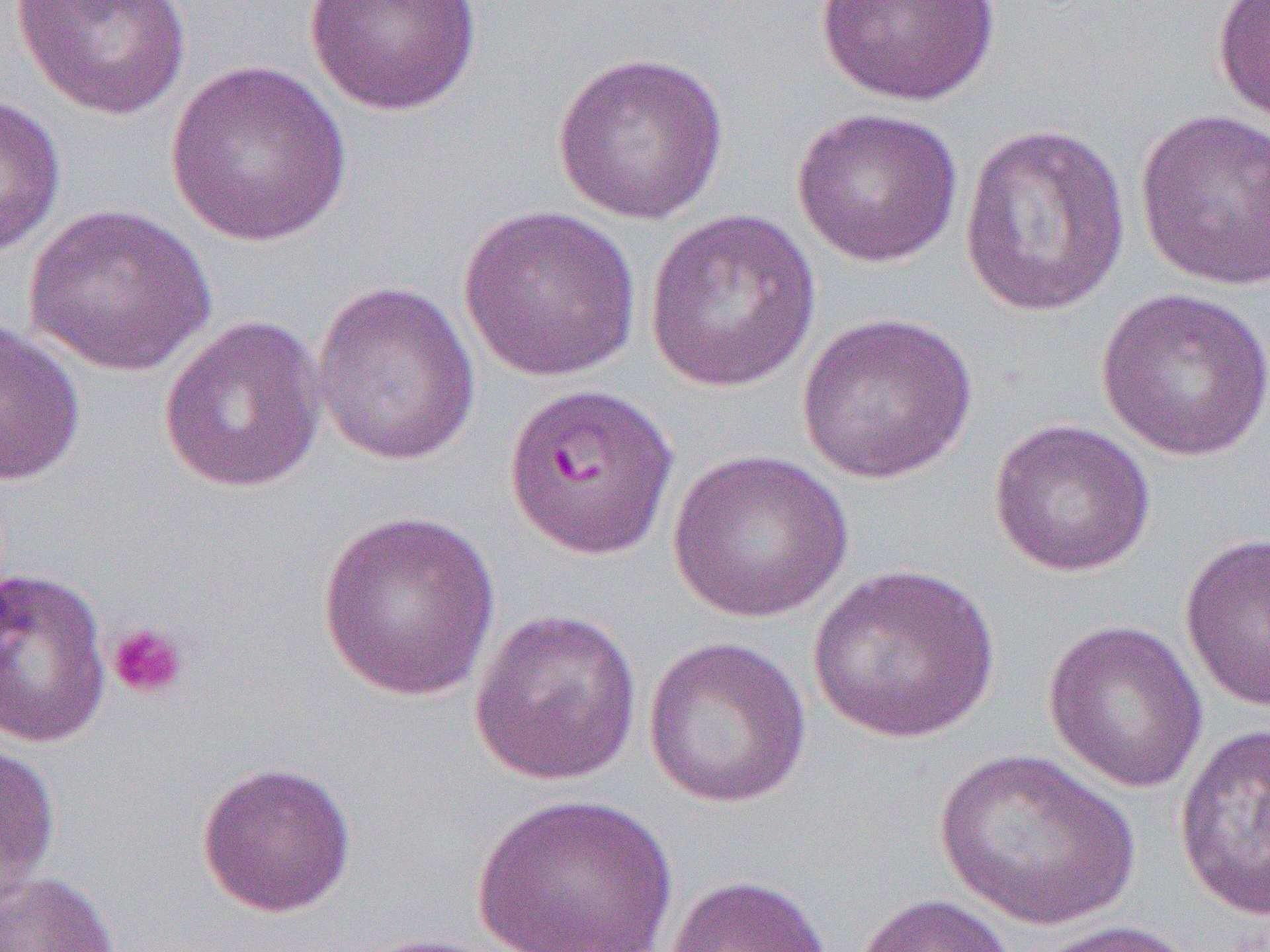

{
  "slide_level_diagnosis": "Plasmodium falciparum",
  "preparation": "thin blood film",
  "uninfected_red_blood_cell_locations": "approximate bounding boxes as (x1, y1, x2, y2) in pixels: (10, 0, 192, 120), (303, 0, 482, 116), (816, 0, 1003, 106), (1211, 0, 1270, 123), (552, 50, 730, 225), (165, 60, 353, 249), (0, 93, 67, 257), (790, 105, 963, 268), (1134, 108, 1270, 291), (959, 122, 1132, 319), (23, 204, 217, 377), (458, 205, 642, 382), (644, 208, 822, 393), (311, 280, 481, 466), (1096, 286, 1270, 461), (795, 312, 978, 484), (158, 315, 328, 494), (0, 317, 86, 486), (987, 418, 1157, 577), (666, 448, 854, 624), (315, 511, 502, 704), (1179, 532, 1270, 713), (806, 564, 1001, 744), (0, 566, 112, 749), (468, 608, 642, 786), (1042, 619, 1209, 794), (642, 636, 813, 809), (1173, 722, 1270, 922), (0, 735, 61, 907), (934, 749, 1142, 931), (195, 760, 357, 918), (471, 792, 679, 952), (0, 868, 121, 952), (663, 873, 835, 952), (851, 893, 1019, 952), (1022, 919, 1198, 952), (355, 932, 516, 952)",
  "modality": "light microscopy",
  "field_of_view": "one of a larger specimen",
  "platelet_locations": "approximate bounding boxes as (x1, y1, x2, y2) in pixels: (106, 622, 189, 700)",
  "image_size": "1270×952 pixels",
  "magnification": "1000x"
}